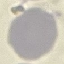 Result: negative for malaria parasites. Cell patch, automatically extracted from a larger field of view and resized to 64 × 64 pixels. Thin blood film. Photographed with a smartphone camera at the microscope eyepiece. Giemsa-stained preparation.